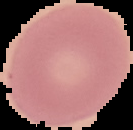

Summary:
  - Image size: 133×130 pixels
  - Preparation: thin blood smear
  - Malaria status: uninfected
  - Image type: segmented cell region on a black background